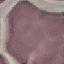

Summary:
  - Result: no malaria parasites detected
  - Image type: cell patch, automatically extracted from a larger field of view and resized to 64 × 64 pixels
  - Preparation: thin smear
  - Stain: Giemsa
  - Capture: smartphone camera at the microscope eyepiece